Classify this cell by malaria status.
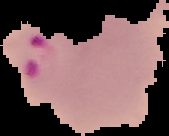

Parasitized.

Cell region segmented out of the field of view; the surrounding area is masked to black. Image is 169×136 pixels. From a thin blood film.